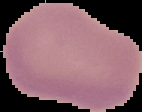
image size = 142×112 pixels
malaria status = uninfected
image type = segmented cell region on a black background
preparation = thin blood smear